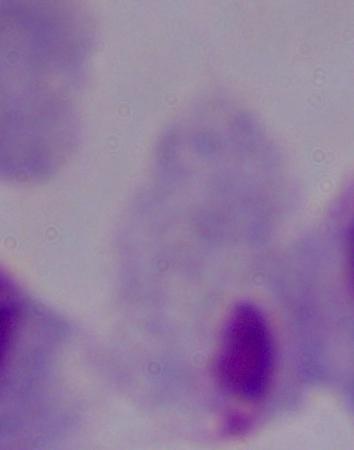
magnification = 1000x
identification = trichomonad
modality = photomicrograph